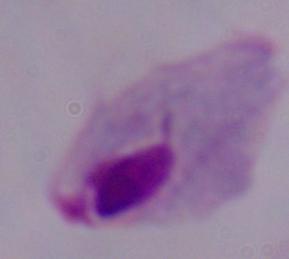 Micrograph. Captured at 1000x magnification. A trichomonad is seen.